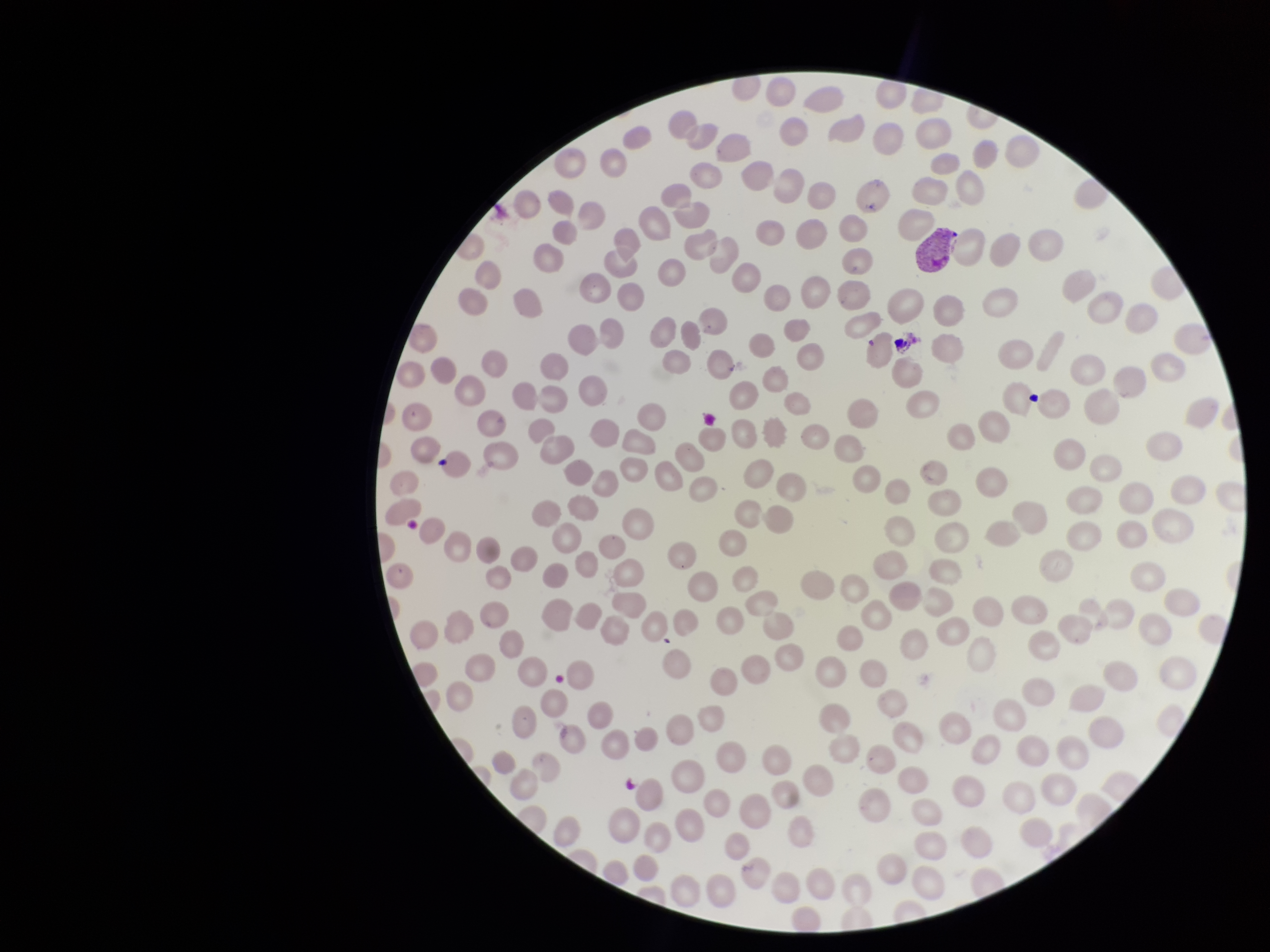
Giemsa stain. Parasitized red blood cells: seen. Preparation: thin blood smear. Image is 1270×952 pixels. One field from this slide. Species reported for this patient: Plasmodium vivax. Red blood cell count: 222. Photographed through the microscope eyepiece with a smartphone camera. Patient malaria status: positive. Parasitized red blood cell count: 1.